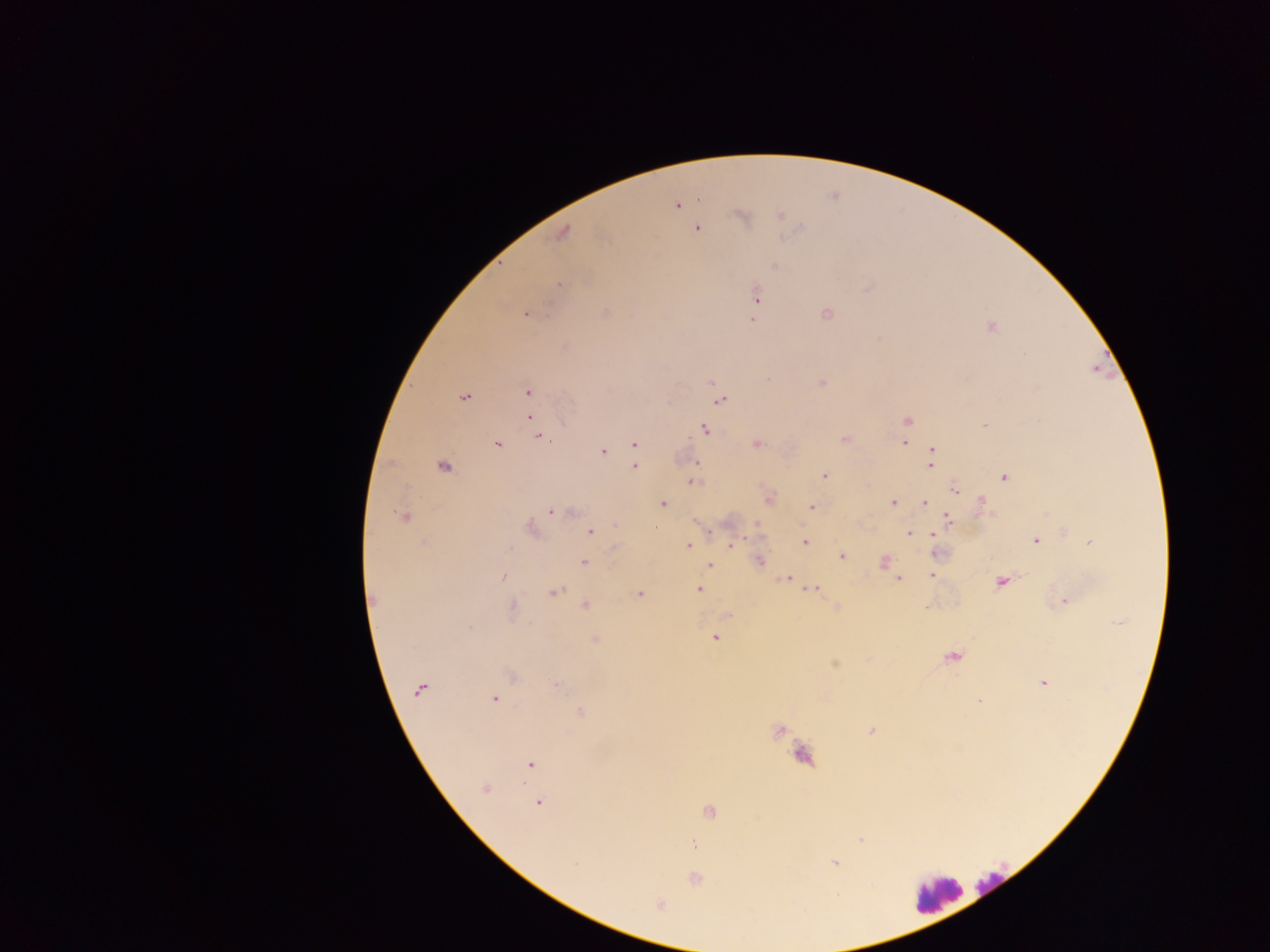
Approximate centers as {x, y} in pixels.
Summary:
  - Leukocyte locations: {989, 884}, {935, 893}
  - Plasmodium parasite locations: {677, 205}, {780, 215}, {741, 217}, {697, 228}, {563, 233}, {775, 266}, {559, 285}, {756, 296}, {754, 309}, {605, 312}, {826, 314}, {525, 315}, {752, 319}, {990, 326}, {769, 379}, {711, 382}, {822, 382}, {528, 393}, {463, 397}, {720, 400}, {530, 418}, {906, 421}, {984, 426}, {705, 430}, {541, 438}, {844, 438}, {904, 443}, {634, 444}, {497, 445}, {757, 445}, {932, 449}, {603, 452}, {696, 463}, {443, 466}, {930, 466}, {635, 467}, {824, 476}, {1004, 477}, {693, 482}, {955, 490}, {768, 498}, {982, 500}, {893, 502}, {924, 502}, {663, 504}, {812, 507}, {550, 512}, {403, 517}, {948, 519}, {756, 523}, {614, 524}, {529, 528}, {710, 532}, {590, 533}, {909, 533}, {932, 534}, {805, 541}, {1035, 541}, {1091, 542}, {732, 545}, {688, 546}, {615, 548}, {842, 556}, {759, 561}, {583, 562}, {884, 562}, {710, 565}, {932, 575}, {502, 577}, {785, 578}, {898, 578}, {1000, 582}, {700, 589}, {811, 589}, {554, 592}, {639, 594}, {373, 599}, {1065, 602}, {586, 605}, {513, 606}, {926, 608}, {728, 615}, {1120, 622}, {469, 628}, {715, 638}, {595, 639}, {953, 657}, {835, 664}, {512, 676}, {1044, 683}, {556, 684}, {420, 689}, {494, 699}, {978, 700}, {581, 713}, {779, 731}, {871, 731}, {530, 764}, {485, 788}, {538, 803}, {710, 811}, {860, 840}, {693, 845}, {834, 863}, {574, 864}, {695, 879}, {660, 905}
  - Capture: mobile-phone photograph through a microscope
  - Country: Ghana
  - Image size: 1270×952 pixels
  - Preparation: thick blood film
  - Field of view: single